Identify the blood parasite species.
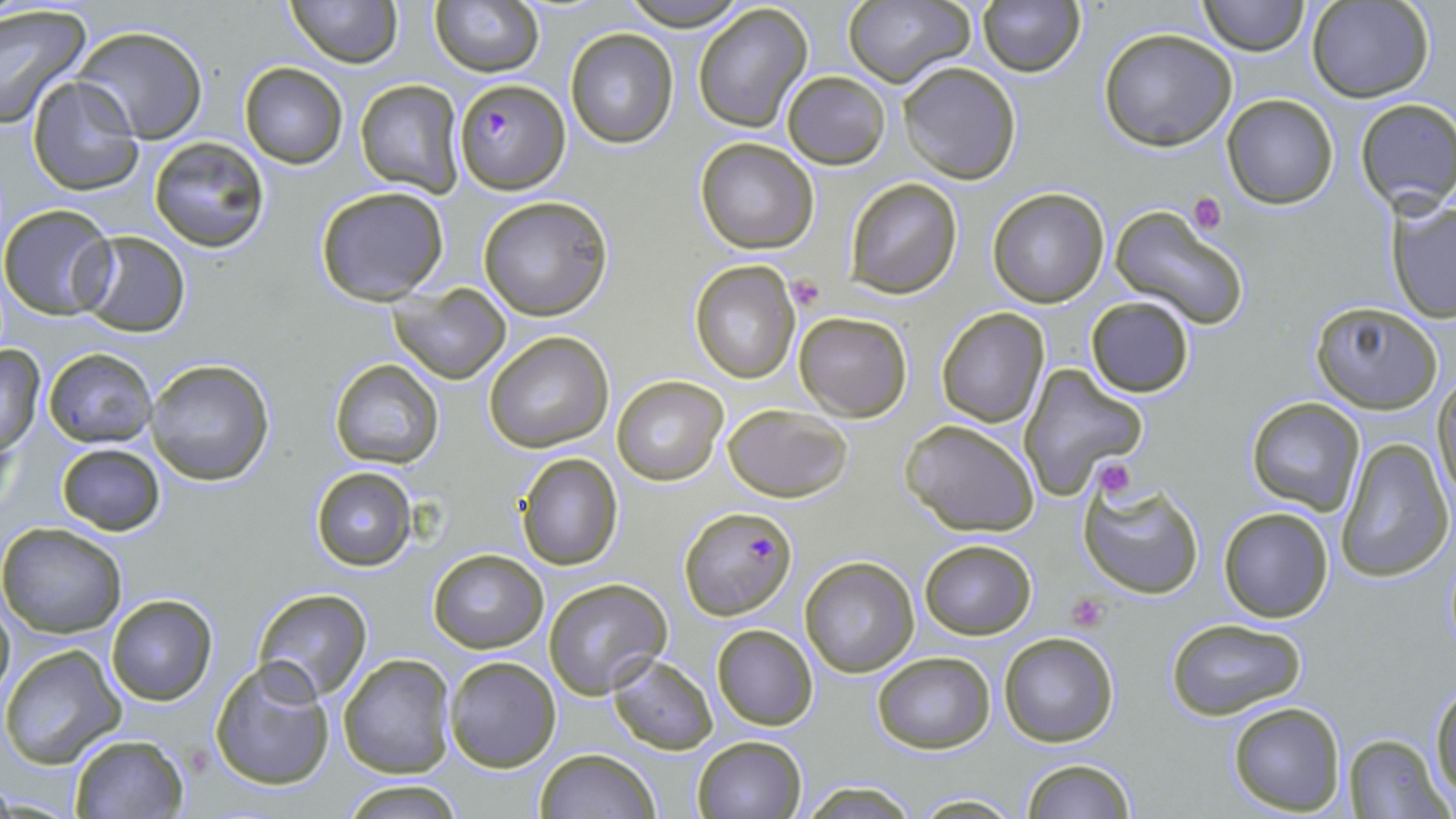
Plasmodium falciparum.

Approximate bounding boxes as named x1/y1/x2/y2 corners in pixels. Uninfected red blood cell locations: (x1=283, y1=0, x2=401, y2=68), (x1=428, y1=0, x2=542, y2=76), (x1=618, y1=0, x2=750, y2=30), (x1=840, y1=0, x2=975, y2=89), (x1=1197, y1=0, x2=1308, y2=55), (x1=1308, y1=0, x2=1433, y2=101), (x1=977, y1=1, x2=1085, y2=77), (x1=0, y1=4, x2=89, y2=129), (x1=692, y1=4, x2=814, y2=132), (x1=71, y1=25, x2=210, y2=144), (x1=565, y1=28, x2=679, y2=148), (x1=1099, y1=28, x2=1238, y2=150), (x1=900, y1=61, x2=1020, y2=184), (x1=239, y1=63, x2=348, y2=167), (x1=782, y1=71, x2=891, y2=168), (x1=25, y1=75, x2=144, y2=194), (x1=354, y1=79, x2=466, y2=196), (x1=1222, y1=94, x2=1339, y2=208), (x1=1354, y1=99, x2=1456, y2=211), (x1=148, y1=136, x2=271, y2=252), (x1=694, y1=136, x2=820, y2=255), (x1=843, y1=177, x2=964, y2=298), (x1=314, y1=185, x2=451, y2=306), (x1=987, y1=187, x2=1111, y2=308), (x1=478, y1=196, x2=614, y2=321), (x1=1387, y1=196, x2=1456, y2=322), (x1=0, y1=204, x2=118, y2=319), (x1=1109, y1=205, x2=1247, y2=329), (x1=77, y1=231, x2=192, y2=338), (x1=689, y1=261, x2=800, y2=382), (x1=390, y1=284, x2=511, y2=384), (x1=1083, y1=295, x2=1196, y2=399), (x1=1308, y1=302, x2=1444, y2=415), (x1=936, y1=308, x2=1049, y2=428), (x1=793, y1=311, x2=912, y2=421), (x1=483, y1=331, x2=615, y2=452), (x1=0, y1=344, x2=46, y2=453), (x1=43, y1=347, x2=155, y2=448), (x1=328, y1=357, x2=445, y2=468), (x1=144, y1=358, x2=275, y2=486), (x1=1017, y1=365, x2=1148, y2=499), (x1=1433, y1=373, x2=1456, y2=508), (x1=612, y1=375, x2=727, y2=485), (x1=1245, y1=396, x2=1365, y2=515), (x1=721, y1=404, x2=852, y2=502), (x1=899, y1=419, x2=1041, y2=536), (x1=1336, y1=437, x2=1453, y2=582), (x1=56, y1=442, x2=167, y2=535), (x1=515, y1=451, x2=625, y2=571), (x1=309, y1=467, x2=417, y2=569), (x1=1077, y1=478, x2=1205, y2=602), (x1=1218, y1=506, x2=1334, y2=622), (x1=0, y1=522, x2=128, y2=639), (x1=918, y1=538, x2=1036, y2=639), (x1=427, y1=547, x2=549, y2=654), (x1=800, y1=556, x2=919, y2=677), (x1=543, y1=578, x2=673, y2=700), (x1=253, y1=587, x2=373, y2=701), (x1=106, y1=594, x2=217, y2=705), (x1=0, y1=597, x2=14, y2=700), (x1=1165, y1=615, x2=1310, y2=722), (x1=711, y1=623, x2=817, y2=731), (x1=1000, y1=631, x2=1119, y2=748), (x1=1, y1=643, x2=127, y2=769), (x1=872, y1=652, x2=996, y2=753), (x1=339, y1=654, x2=455, y2=778), (x1=608, y1=654, x2=718, y2=754), (x1=443, y1=655, x2=561, y2=772), (x1=211, y1=661, x2=334, y2=789), (x1=1431, y1=681, x2=1456, y2=803), (x1=1226, y1=700, x2=1346, y2=816), (x1=1343, y1=732, x2=1448, y2=817), (x1=69, y1=733, x2=187, y2=817), (x1=691, y1=735, x2=807, y2=818), (x1=536, y1=748, x2=658, y2=819), (x1=1019, y1=757, x2=1136, y2=819), (x1=335, y1=779, x2=470, y2=817), (x1=799, y1=780, x2=923, y2=818), (x1=912, y1=792, x2=1022, y2=817). Plasmodium falciparum-infected red blood cell locations: (x1=452, y1=77, x2=570, y2=194), (x1=677, y1=508, x2=797, y2=621). Platelet locations: (x1=1187, y1=193, x2=1226, y2=236), (x1=786, y1=276, x2=825, y2=312), (x1=1088, y1=456, x2=1139, y2=498), (x1=1067, y1=593, x2=1108, y2=630). Thin blood smear. Optical microscopy. May-Grünwald-Giemsa-stained preparation. One field of a larger specimen. Image is 1456×819 pixels. Captured at 1000x magnification.